Describe the morphology of the red blood cells.
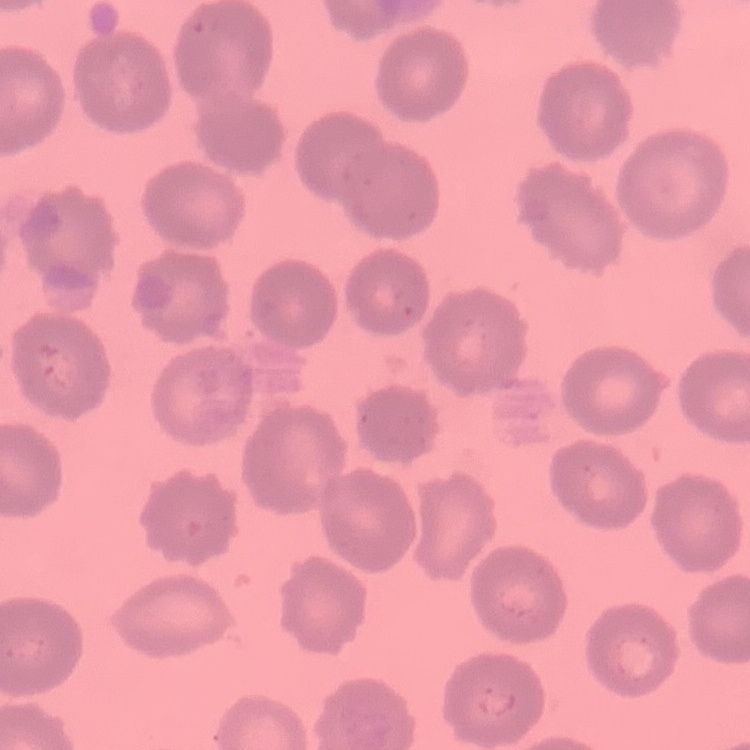
They show no rouleaux formation.

Thin blood film. Field's or Giemsa stain. Square crop of a larger photomicrograph.